Classify this cell by malaria status.
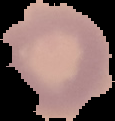

Uninfected.

image_size: 115×121 pixels
image_type: cell region segmented out of the field of view; surrounding area masked to black
preparation: thin blood film